Name the parasite shown.
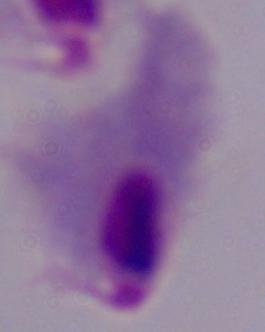

This is a trichomonad.

1000x magnification. Photomicrograph.